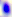

magnification = 400x
identification = Toxoplasma gondii
modality = photomicrograph